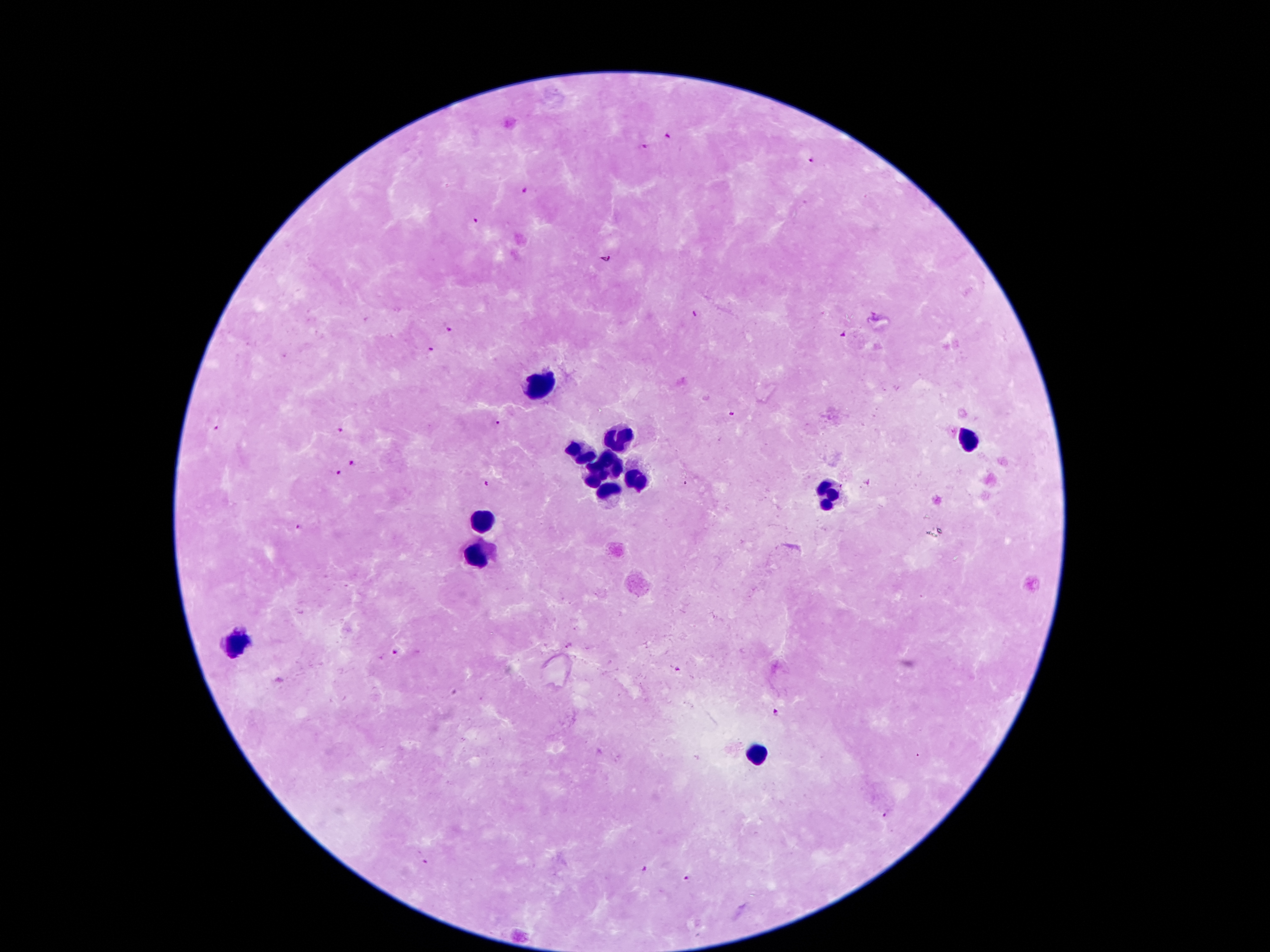
Approximate object centers, in pixels from the top-left corner. Malaria parasite locations: (x=669, y=136), (x=645, y=146), (x=811, y=159), (x=525, y=189), (x=475, y=220), (x=604, y=259), (x=696, y=314), (x=448, y=329), (x=841, y=333), (x=431, y=349), (x=732, y=412), (x=496, y=423), (x=215, y=428), (x=339, y=429), (x=351, y=462), (x=340, y=473), (x=486, y=482), (x=299, y=527), (x=397, y=653), (x=775, y=713), (x=884, y=816), (x=426, y=862), (x=643, y=869), (x=685, y=879). Leukocyte locations: (x=540, y=386), (x=965, y=437), (x=622, y=438), (x=579, y=453), (x=610, y=463), (x=596, y=475), (x=637, y=479), (x=831, y=493), (x=608, y=494), (x=484, y=521), (x=478, y=552), (x=232, y=642), (x=757, y=754). Image is 1270×952 pixels. Patient malaria status: positive for Plasmodium falciparum. 100x magnification. Giemsa stain. Thick peripheral-blood smear. Photographed through the microscope eyepiece with a smartphone camera. One field from this slide.